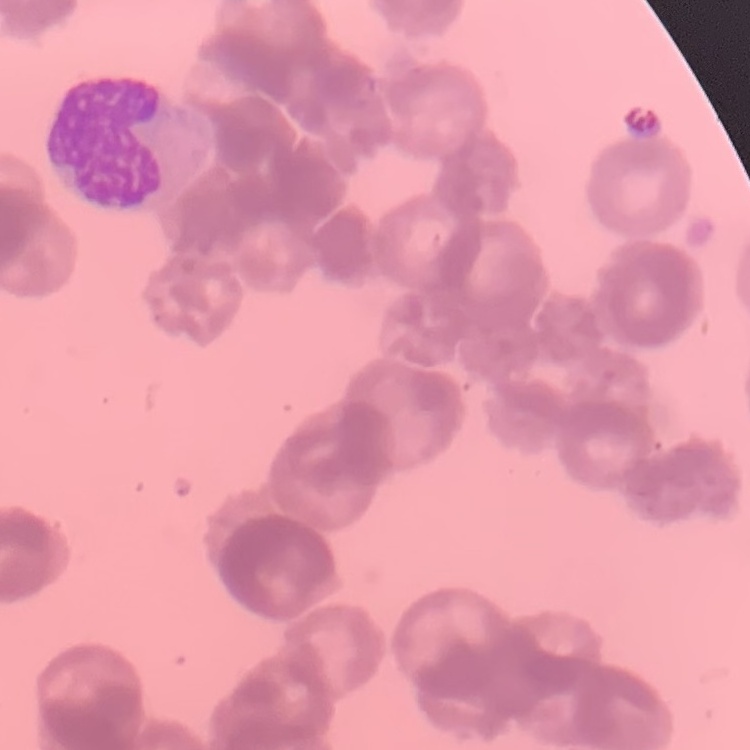
erythrocyte morphology = rouleaux formation
image type = one tile cut from a larger photomicrograph
preparation = thin peripheral smear
stain = Field's or Giemsa